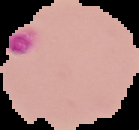

Malaria status: parasitized. The area outside the segmented cell region is set to black. Image is 139×130 pixels. From a thin blood film.